Locate and identify every blood parasite.
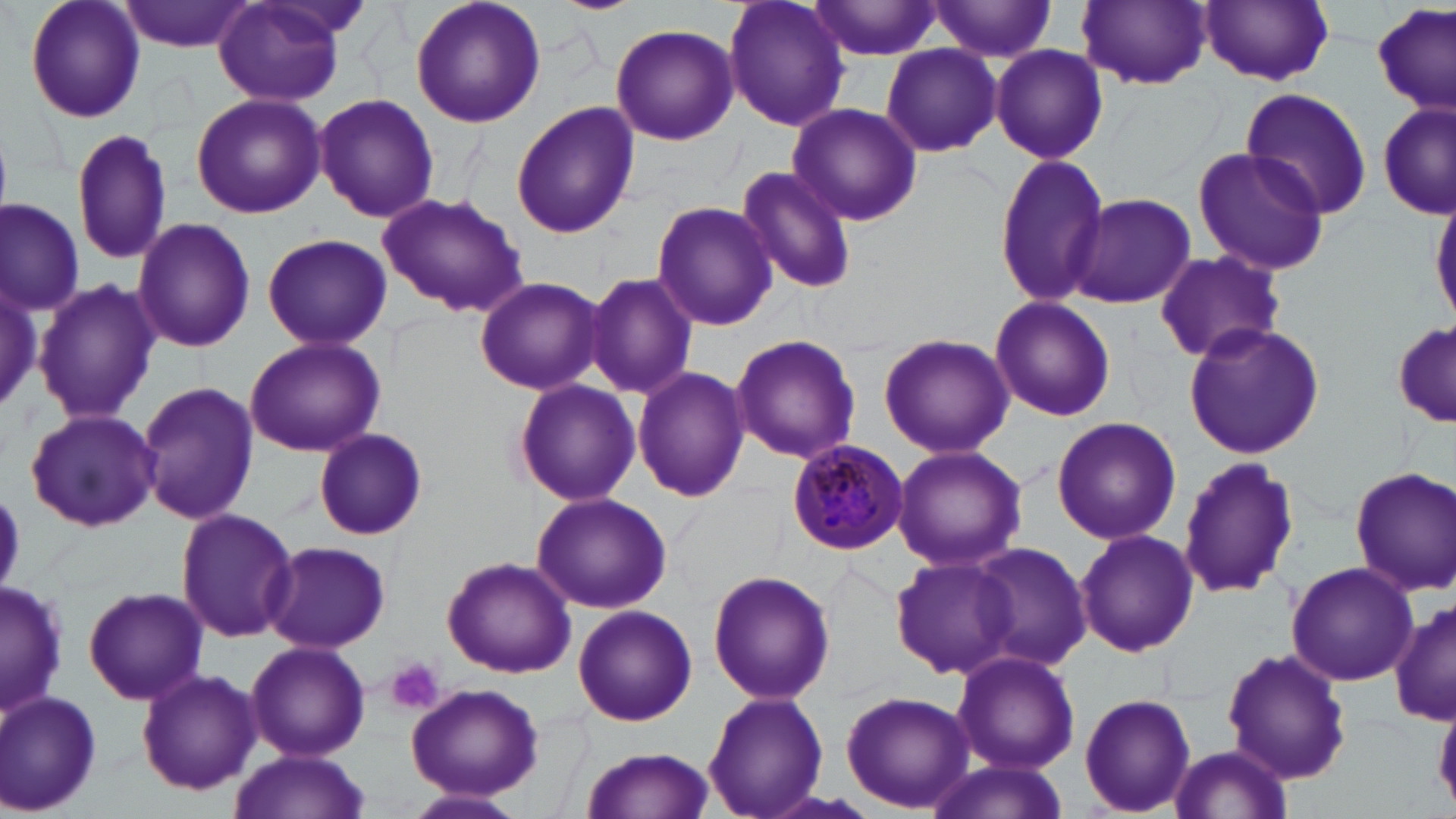

Approximate bounding boxes as (x1, y1, x2, y2) in pixels.
Plasmodium malariae-infected red blood cells: (787, 438, 907, 554).
No Plasmodium falciparum, Plasmodium ovale, Plasmodium vivax, Babesia divergens, or Trypanosoma brucei observed.

Uninfected red blood cell locations: (22, 0, 147, 124), (121, 0, 257, 52), (409, 0, 547, 128), (549, 0, 643, 15), (723, 0, 850, 133), (808, 0, 949, 63), (930, 0, 1060, 62), (1077, 0, 1211, 89), (1199, 0, 1334, 85), (214, 2, 346, 107), (1369, 5, 1453, 113), (609, 23, 738, 144), (989, 43, 1107, 165), (880, 44, 1001, 158), (1240, 87, 1374, 216), (190, 93, 328, 218), (312, 93, 439, 223), (511, 101, 639, 238), (1379, 101, 1453, 221), (787, 102, 922, 227), (69, 128, 175, 266), (1192, 146, 1331, 275), (991, 151, 1111, 308), (734, 164, 857, 294), (376, 192, 529, 317), (1068, 193, 1196, 310), (1431, 193, 1456, 328), (651, 201, 778, 330), (1, 202, 84, 313), (131, 217, 256, 355), (259, 233, 395, 350), (1151, 248, 1285, 365), (585, 272, 698, 398), (0, 273, 52, 421), (474, 276, 602, 395), (34, 278, 158, 425), (989, 297, 1117, 423), (1182, 321, 1324, 458), (1393, 324, 1454, 430), (878, 332, 1014, 459), (730, 333, 862, 464), (244, 336, 385, 457), (633, 366, 750, 504), (512, 378, 640, 506), (137, 380, 257, 525), (25, 408, 161, 533), (1050, 416, 1181, 545), (313, 427, 428, 540), (891, 445, 1027, 572), (1176, 455, 1299, 600), (1351, 465, 1455, 597), (531, 492, 672, 613), (175, 506, 299, 644), (1074, 528, 1199, 658), (262, 540, 393, 655), (970, 541, 1094, 671), (889, 552, 1023, 681), (443, 557, 578, 678), (1286, 561, 1420, 685), (707, 569, 836, 704), (1, 579, 67, 717), (83, 584, 208, 704), (1390, 602, 1455, 727), (573, 605, 697, 726), (245, 640, 370, 761), (1219, 647, 1352, 786), (950, 650, 1080, 774), (135, 668, 262, 795), (405, 683, 545, 802), (0, 689, 103, 816), (703, 691, 828, 818), (839, 691, 975, 813), (1078, 693, 1197, 816), (1166, 743, 1293, 818), (577, 747, 718, 819), (229, 750, 370, 818), (922, 759, 1070, 818), (405, 789, 530, 818). Platelet locations: (385, 656, 444, 715). Slide-level diagnosis: Plasmodium malariae. Thin blood film. Captured at 1000x magnification. Single field of view. May-Grünwald-Giemsa-stained preparation. Image is 1456×819 pixels. Light microscopy.